Describe the morphology of the red blood cells.
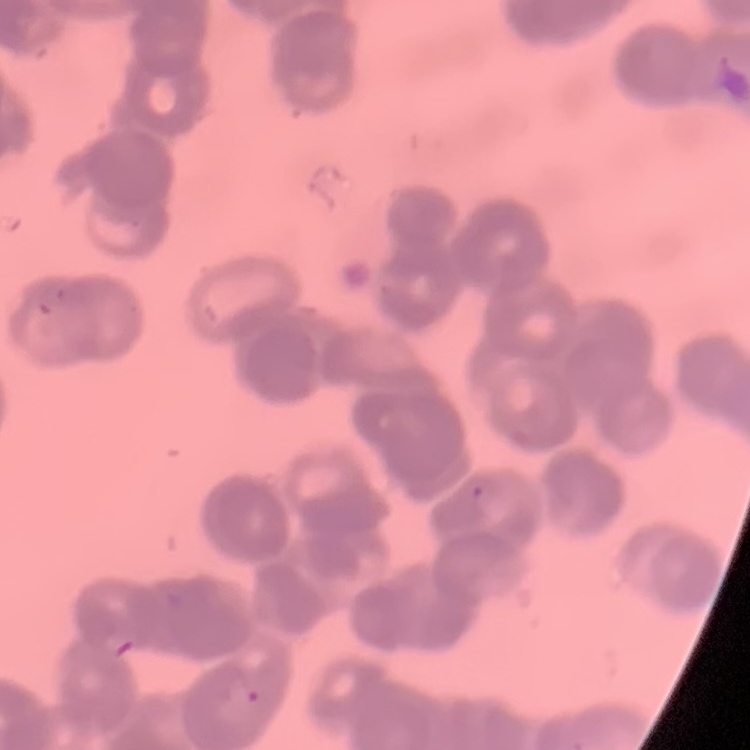
Rouleaux formation.

Summary:
  - Preparation: thin blood film
  - Stain: Field's or Giemsa
  - Image type: one tile cut from a larger photomicrograph